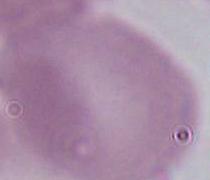
magnification = 1000x
identification = red blood cell
modality = photomicrograph